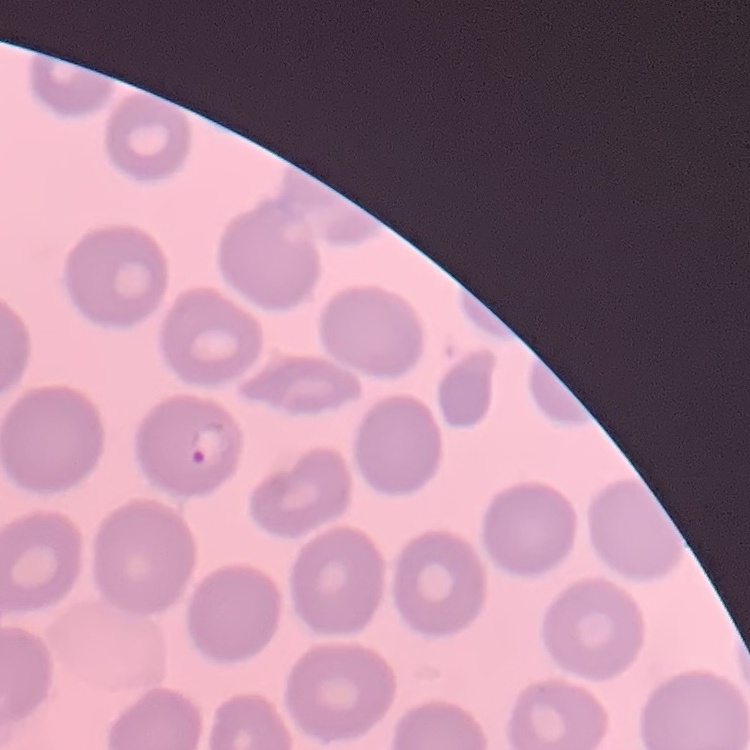
Summary:
  - Erythrocyte morphology: no rouleaux formation
  - Image type: square crop of a larger photomicrograph
  - Preparation: thin peripheral smear
  - Stain: Field's or Giemsa